Give a bounding box for every leukocyte visible.
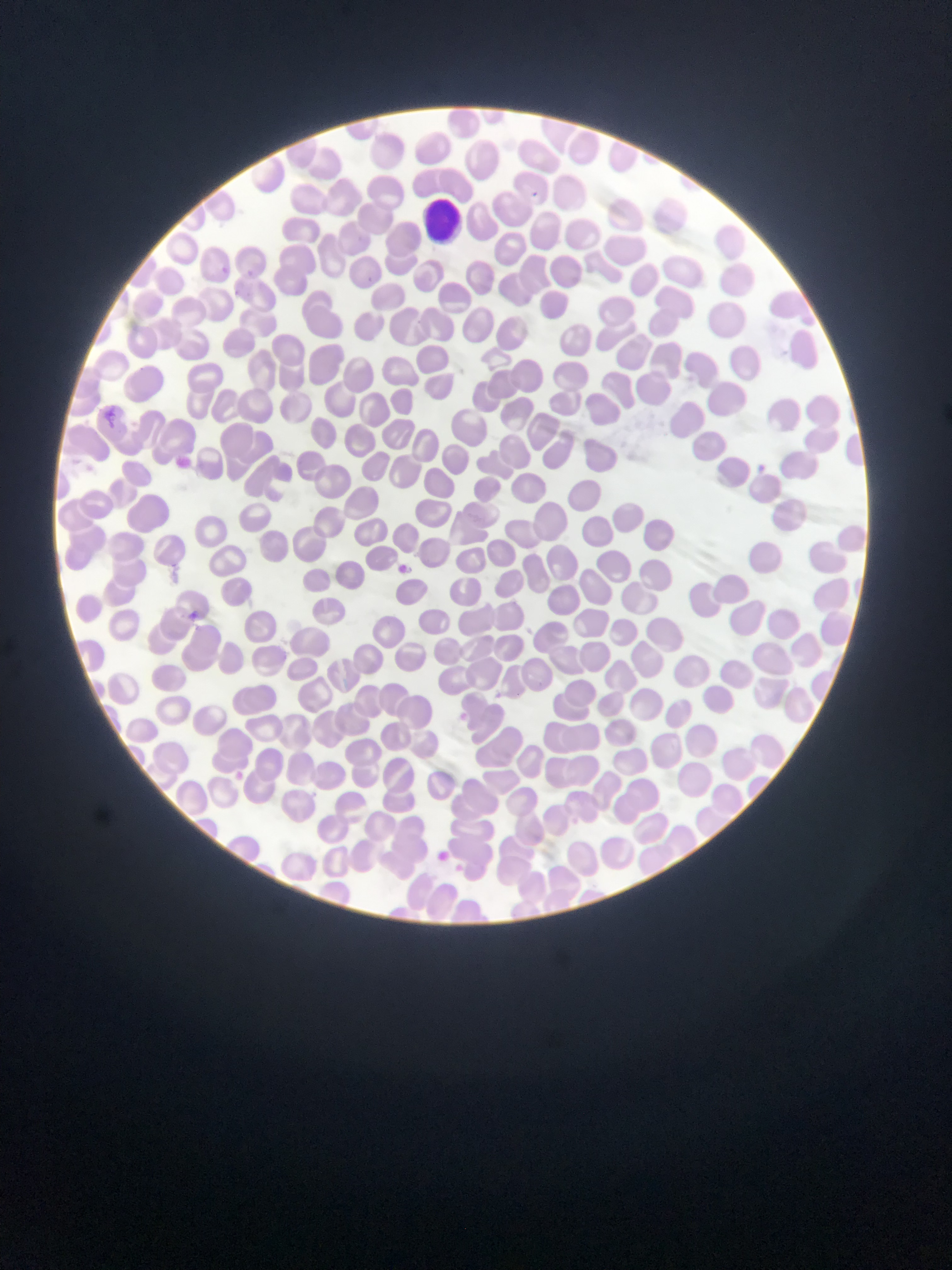
Approximate bounding boxes as (left, top, right, bottom) in pixels.
Leukocytes: (424, 195, 462, 239).

Plasmodium parasite locations: (529, 184, 542, 202), (218, 262, 230, 277), (242, 269, 256, 281), (232, 288, 244, 300), (104, 405, 119, 430), (751, 458, 768, 475), (400, 557, 413, 576), (184, 609, 203, 625), (232, 766, 243, 782), (437, 847, 449, 861). Image is 952×1270 pixels. Thin blood film. Sample from Ghana. One field of view. Photographed through a microscope with a mobile-phone camera.